State which parasite is depicted.
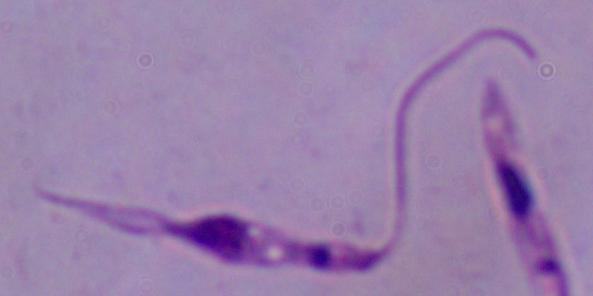
This is Leishmania.

Captured at 1000x magnification. Photomicrograph.